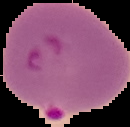
From a thin blood film. Image is 130×127 pixels. Segmented cell region on a black background. Malaria status: parasitized.